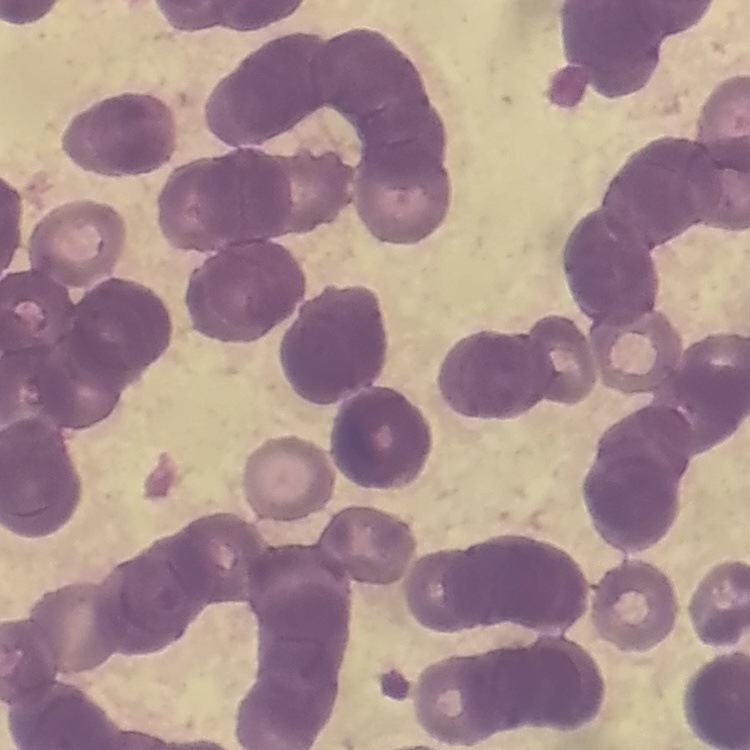
{
  "red_blood_cell_morphology": "rouleaux formation",
  "image_type": "square crop of a larger photomicrograph",
  "preparation": "thin peripheral smear",
  "stain": "Field's or Giemsa"
}